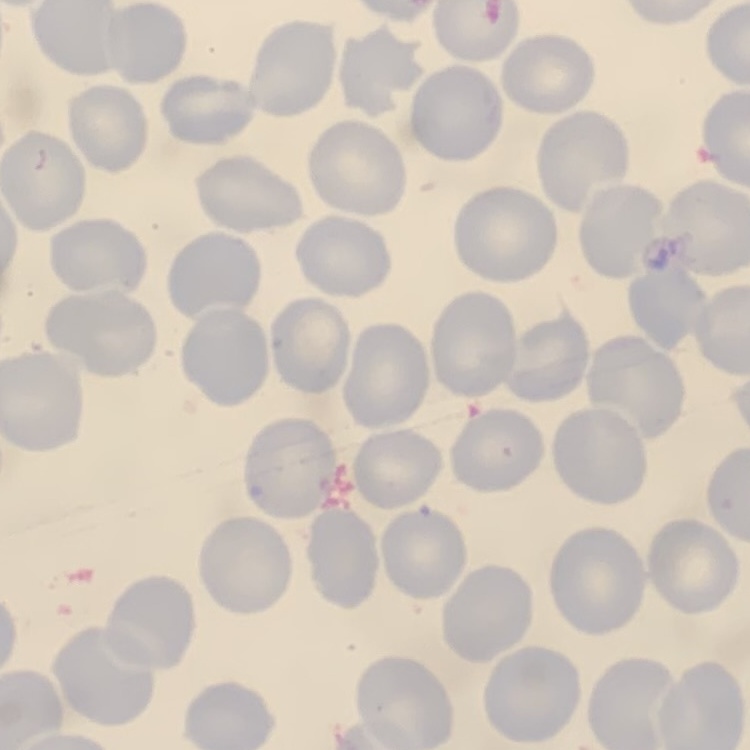
The red blood cells exhibit no rouleaux formation. Thin peripheral smear. Stained with either Field's or Giemsa. Square crop of a larger photomicrograph.